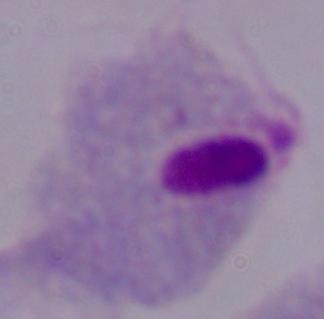

{
  "magnification": "1000x",
  "identification": "trichomonad",
  "modality": "photomicrograph"
}